Assess the morphology of the red blood cells.
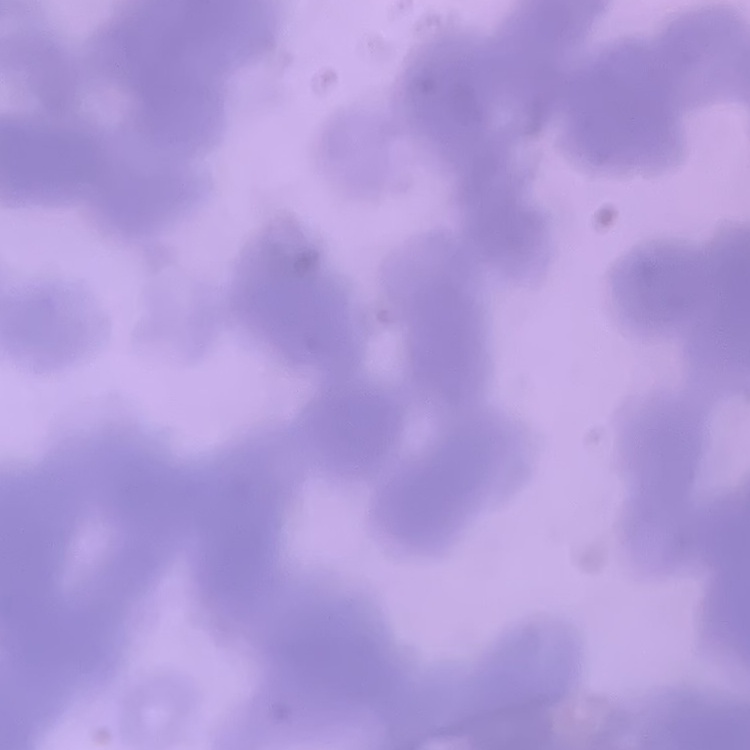
Rouleaux formation.

Field's or Giemsa stain. One tile cut from a larger photomicrograph. Thin blood smear.